Locate every parasitized RBC.
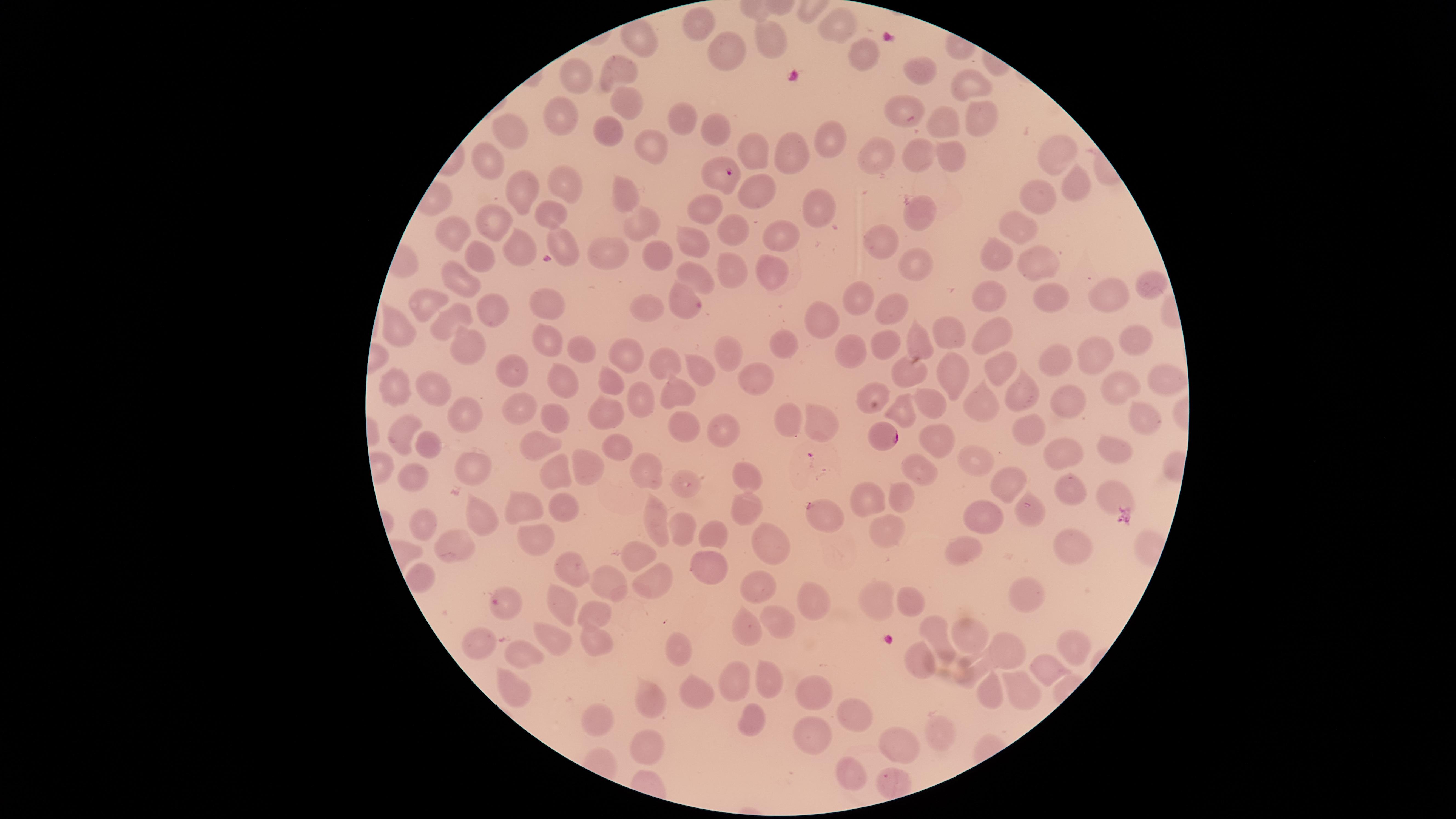

Approximate marker points as [x, y] in pixels.
Parasitized RBCs: [727, 174], [886, 439], [815, 513].

Approximate marker points as [x, y] in pixels.
Summary:
  - Uninfected RBCs: [830, 17], [702, 18], [642, 39], [722, 50], [760, 50], [861, 50], [622, 72], [919, 72], [968, 82], [581, 83], [625, 104], [907, 114], [560, 120], [949, 120], [981, 120], [679, 122], [716, 130], [507, 132], [607, 133], [831, 139], [652, 144], [752, 152], [796, 152], [883, 154], [919, 154], [1052, 156], [954, 157], [485, 166], [566, 178], [529, 183], [1081, 183], [759, 192], [623, 193], [1047, 198], [702, 204], [809, 204], [548, 210], [915, 211], [491, 225], [640, 225], [1025, 225], [736, 228], [456, 233], [781, 238], [563, 241], [882, 241], [518, 246], [692, 247], [1007, 247], [658, 249], [609, 251], [474, 256], [1033, 257], [914, 259], [769, 269], [727, 271], [696, 275], [462, 282], [1151, 286], [997, 291], [1102, 291], [1041, 294], [685, 298], [854, 298], [545, 301], [651, 304], [896, 305], [492, 310], [427, 313], [452, 321], [816, 323], [393, 328], [946, 331], [997, 333], [552, 334], [468, 338], [1136, 342], [776, 343], [918, 343], [886, 344], [577, 347], [844, 349], [722, 353], [622, 354], [1055, 356], [1101, 358], [669, 361], [1002, 363], [513, 366], [698, 370], [953, 370], [562, 374], [761, 376], [909, 376], [1155, 380], [676, 384], [1114, 384], [607, 386], [398, 388], [432, 390], [870, 392], [1018, 395], [1066, 400], [975, 404], [638, 405], [937, 405], [906, 409], [524, 412], [468, 414], [599, 415], [552, 417], [790, 417], [684, 418], [1138, 423], [717, 424], [823, 424], [1028, 429], [406, 432], [936, 439], [539, 444], [428, 445], [612, 445], [1058, 452], [1116, 452], [975, 459], [589, 467], [647, 470], [916, 471], [474, 472], [554, 473], [413, 475], [748, 475], [685, 485], [1009, 485], [1073, 490], [864, 493], [1117, 495], [898, 499], [525, 502], [746, 502], [564, 508], [1033, 512], [479, 516], [656, 516], [983, 517], [421, 523], [678, 531], [880, 531], [536, 536], [708, 538], [773, 539], [464, 540], [641, 550], [957, 550], [1074, 553], [707, 562], [571, 571], [653, 577], [614, 581], [761, 584], [1032, 595], [875, 596], [906, 598], [812, 600], [597, 607], [563, 609], [505, 610], [776, 625], [745, 630], [939, 635], [553, 636], [596, 639], [967, 642], [673, 643], [478, 645], [1073, 647], [525, 651], [921, 653], [1007, 653], [978, 669], [1049, 669], [733, 679], [770, 683], [814, 683], [699, 689], [1016, 691], [991, 695], [512, 696], [654, 701], [601, 715], [853, 715], [753, 719], [811, 737], [644, 739], [928, 739], [892, 745], [851, 774], [891, 786]
  - Field of view: single
  - Preparation: thin blood film
  - Species: Plasmodium falciparum
  - Visible region: circular
  - Capture: smartphone photograph through the microscope eyepiece
  - Image size: 1456×819 pixels
  - Stain: Giemsa